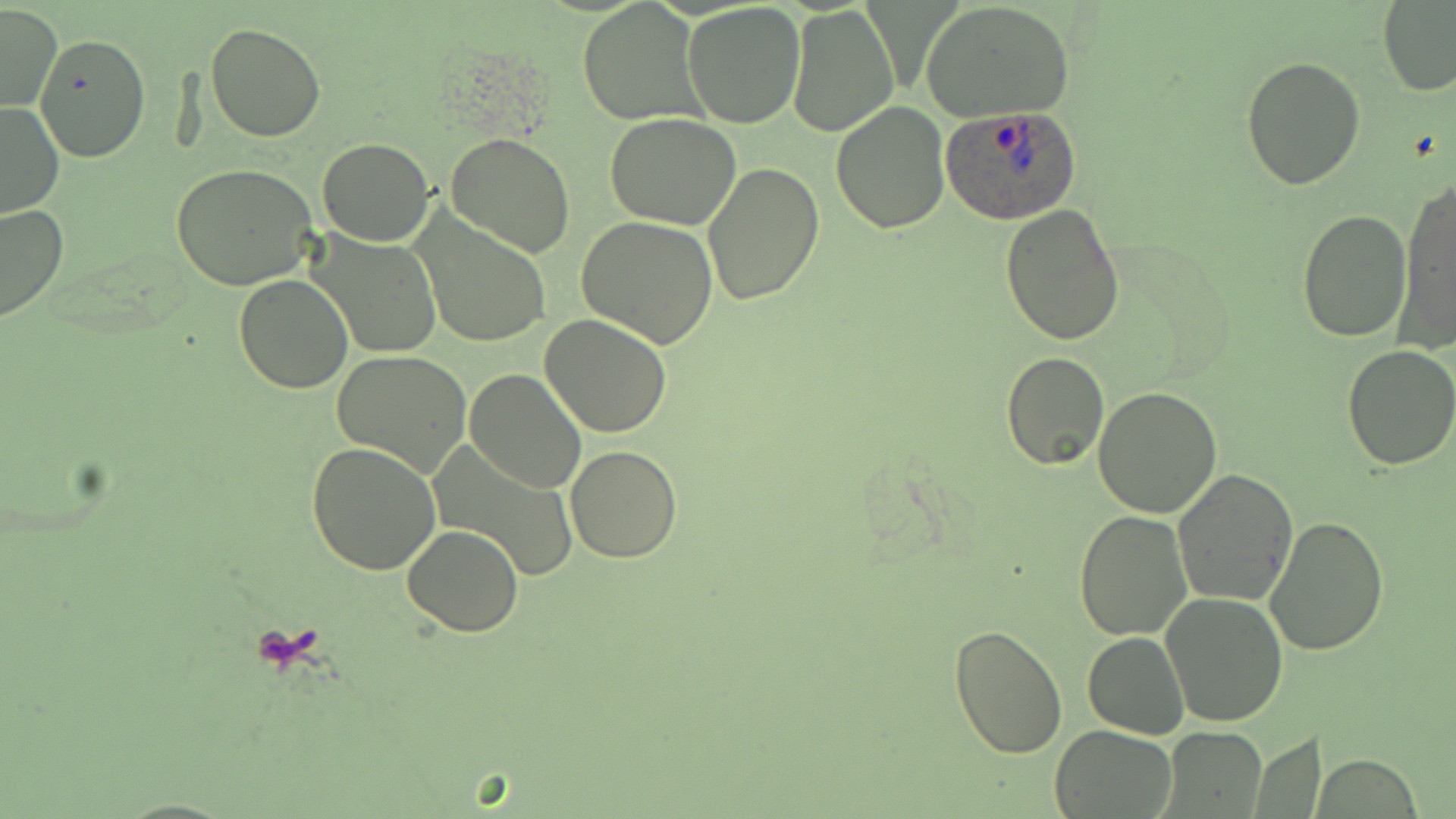
Summary:
  - Coordinate format: approximate bounding boxes as (x1, y1, x2, y2) in pixels
  - Plasmodium ovale-infected red blood cell locations: (938, 107, 1084, 224)
  - Uninfected red blood cell locations: (578, 0, 706, 127), (921, 1, 1075, 122), (683, 2, 807, 128), (1378, 2, 1456, 96), (1, 3, 62, 113), (787, 3, 899, 137), (205, 22, 327, 142), (35, 33, 149, 162), (1241, 57, 1366, 190), (829, 100, 950, 233), (0, 102, 63, 220), (605, 112, 742, 230), (445, 132, 577, 260), (316, 138, 435, 247), (700, 161, 824, 307), (171, 163, 319, 290), (1397, 175, 1456, 354), (0, 201, 70, 323), (999, 202, 1125, 344), (1296, 208, 1413, 342), (411, 211, 552, 350), (576, 216, 718, 349), (313, 233, 444, 360), (234, 272, 353, 394), (539, 313, 671, 440), (1341, 346, 1456, 470), (331, 350, 472, 477), (1002, 350, 1109, 470), (464, 368, 585, 492), (1092, 387, 1224, 519), (307, 442, 442, 575), (428, 442, 578, 582), (566, 446, 681, 563), (1171, 468, 1299, 607), (1074, 510, 1191, 642), (1265, 515, 1389, 657), (404, 524, 525, 638), (1161, 592, 1288, 728), (948, 624, 1068, 760), (1084, 632, 1188, 739), (1049, 726, 1178, 819), (1164, 727, 1265, 813)
  - Slide-level diagnosis: Plasmodium ovale
  - Modality: light microscopy
  - Magnification: 1000x
  - Stain: May-Grünwald-Giemsa
  - Image size: 1456×819 pixels
  - Field of view: one of a larger specimen
  - Preparation: thin blood smear